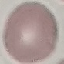

malaria status = uninfected
stain = Giemsa
capture = smartphone camera at the microscope eyepiece
image type = cell patch, automatically extracted from a larger field of view and resized to 64 × 64 pixels
preparation = thin smear